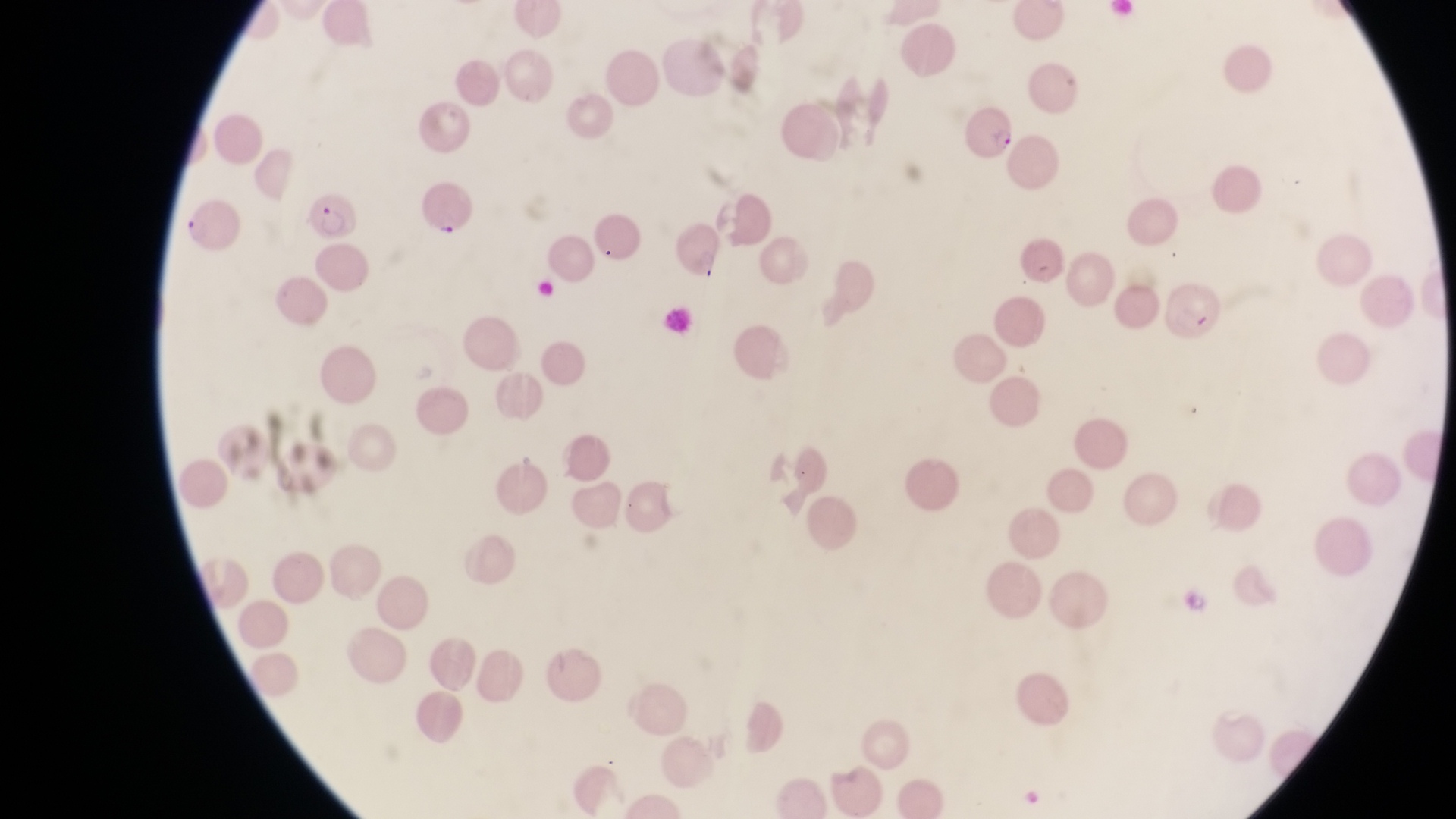
Approximate bounding boxes as {left, top, right, bottom} in pixels.
Summary:
  - Parasitised red blood cell locations: {964, 103, 1017, 162}, {415, 172, 473, 235}, {303, 190, 359, 243}, {180, 201, 239, 250}, {1021, 232, 1064, 288}, {1171, 281, 1227, 347}
  - Field of view: single
  - Preparation: thin blood smear
  - Image size: 1456×819 pixels
  - Country: Uganda
  - Magnification: 1000x
  - Capture: smartphone photograph through the eyepiece of an Olympus CX-23 microscope